Comment on the morphology of the red blood cells.
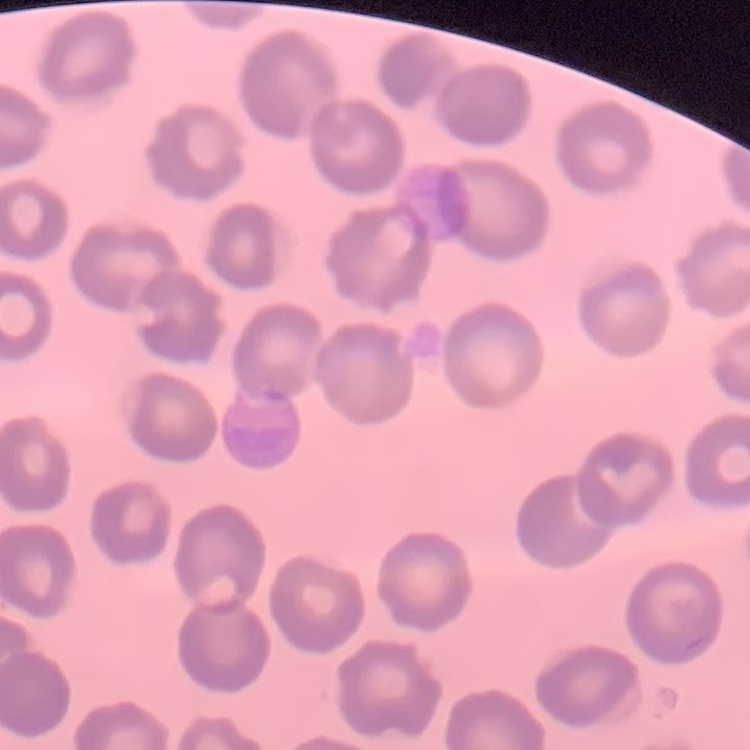

No rouleaux formation.

preparation = thin blood film
stain = Field's or Giemsa
image type = square crop of a larger photomicrograph